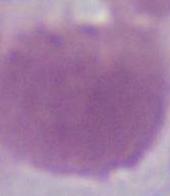
modality = photomicrograph
magnification = 1000x
identification = red blood cell